Locate every Plasmodium parasite and every leukocyte.
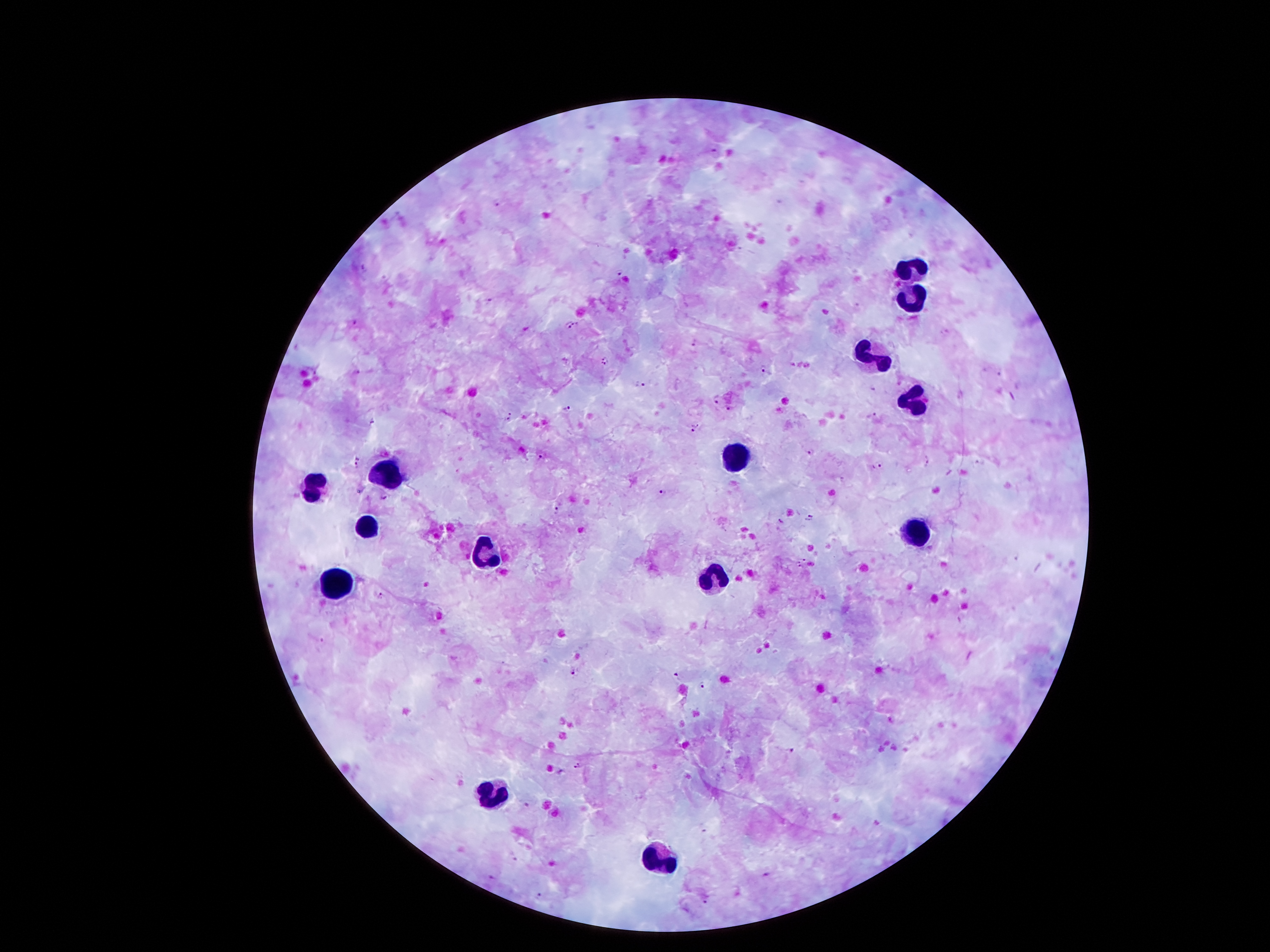

Approximate object centers, in pixels from the top-left corner.
Plasmodium parasites: (x=715, y=152), (x=497, y=202), (x=619, y=272), (x=488, y=299), (x=857, y=306), (x=356, y=321), (x=575, y=324), (x=566, y=326), (x=947, y=332), (x=694, y=341), (x=603, y=362), (x=764, y=371), (x=999, y=373), (x=639, y=383), (x=717, y=400), (x=730, y=407), (x=567, y=408), (x=508, y=414), (x=872, y=414), (x=695, y=428), (x=812, y=451), (x=541, y=455), (x=358, y=460), (x=979, y=462), (x=925, y=463), (x=878, y=467), (x=661, y=493), (x=384, y=498), (x=557, y=509), (x=810, y=518), (x=779, y=521), (x=804, y=559), (x=798, y=566), (x=381, y=596), (x=574, y=672), (x=678, y=675), (x=703, y=687), (x=792, y=751), (x=579, y=765), (x=562, y=770), (x=491, y=875), (x=767, y=875), (x=540, y=895), (x=706, y=902).
Leukocytes: (x=913, y=270), (x=911, y=297), (x=870, y=359), (x=911, y=400), (x=731, y=461), (x=391, y=477), (x=316, y=486), (x=366, y=527), (x=920, y=531), (x=484, y=556), (x=718, y=577), (x=336, y=583), (x=493, y=794), (x=659, y=860).

preparation = thick peripheral-blood smear
magnification = 100x
image size = 1270×952 pixels
capture = smartphone through the microscope eyepiece
field of view = single
stain = Giemsa
patient malaria status = infected with Plasmodium falciparum